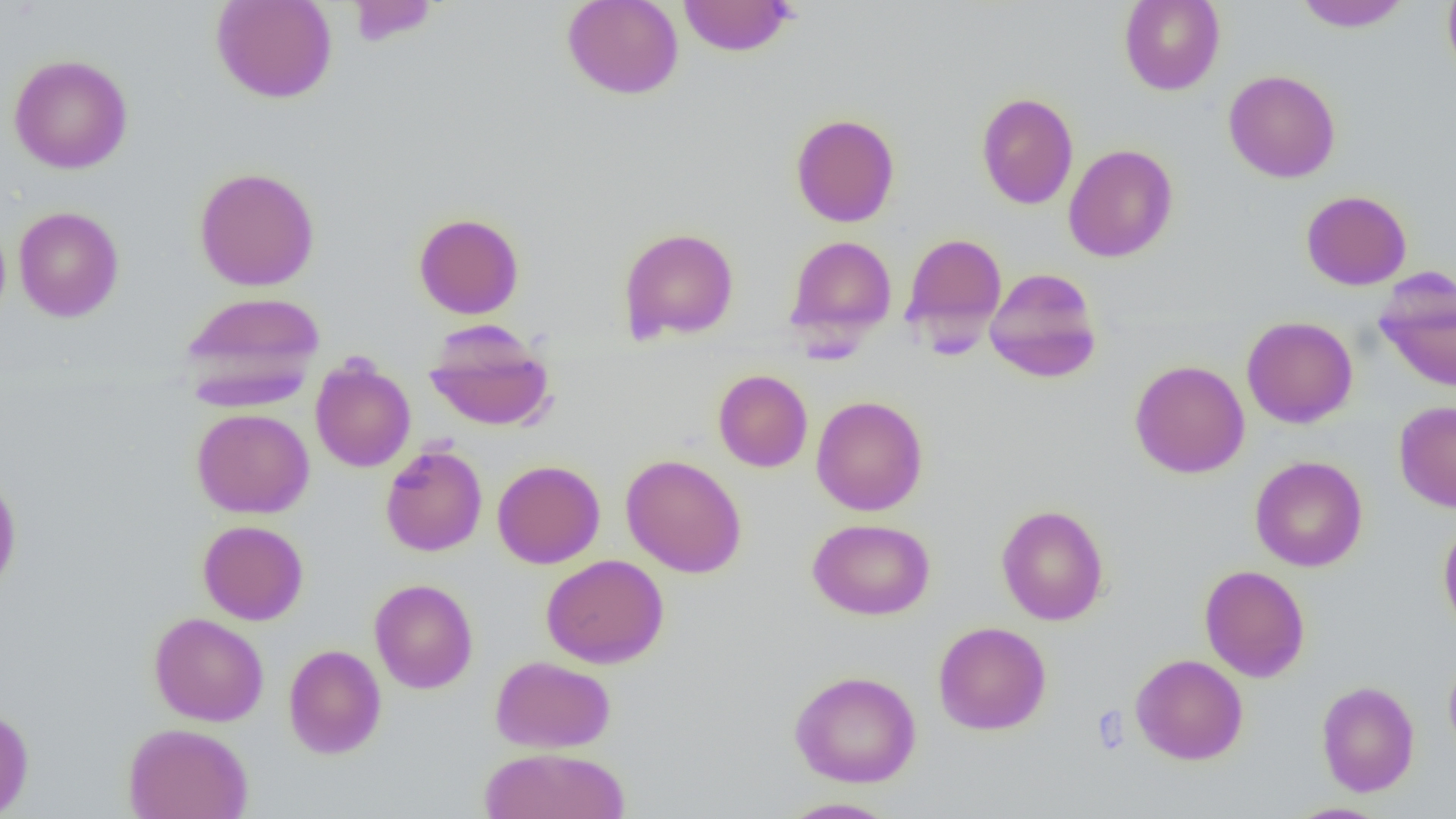

slide-level diagnosis = no evidence of blood parasites
platelet locations = approximate bounding boxes as named x1/y1/x2/y2 corners in pixels: (x1=1090, y1=705, x2=1130, y2=754)
preparation = thin blood film
modality = light microscopy
field of view = single
uninfected red blood cell locations = approximate bounding boxes as named x1/y1/x2/y2 corners in pixels: (x1=210, y1=0, x2=337, y2=104), (x1=561, y1=0, x2=684, y2=100), (x1=677, y1=0, x2=796, y2=57), (x1=1118, y1=0, x2=1225, y2=95), (x1=1294, y1=0, x2=1410, y2=31), (x1=1442, y1=0, x2=1456, y2=84), (x1=346, y1=1, x2=440, y2=46), (x1=8, y1=54, x2=133, y2=174), (x1=1223, y1=69, x2=1341, y2=183), (x1=976, y1=91, x2=1079, y2=210), (x1=790, y1=114, x2=900, y2=227), (x1=1063, y1=143, x2=1178, y2=262), (x1=194, y1=166, x2=320, y2=291), (x1=1301, y1=190, x2=1412, y2=290), (x1=13, y1=206, x2=124, y2=322), (x1=413, y1=212, x2=524, y2=319), (x1=618, y1=227, x2=739, y2=342), (x1=901, y1=232, x2=1007, y2=341), (x1=785, y1=235, x2=897, y2=343), (x1=984, y1=267, x2=1103, y2=383), (x1=1375, y1=273, x2=1456, y2=392), (x1=180, y1=290, x2=325, y2=401), (x1=1242, y1=316, x2=1358, y2=428), (x1=423, y1=322, x2=555, y2=432), (x1=310, y1=357, x2=415, y2=472), (x1=1130, y1=359, x2=1250, y2=479), (x1=713, y1=369, x2=812, y2=473), (x1=811, y1=395, x2=928, y2=516), (x1=1394, y1=401, x2=1456, y2=512), (x1=192, y1=408, x2=314, y2=518), (x1=381, y1=444, x2=487, y2=556), (x1=621, y1=453, x2=747, y2=578), (x1=1250, y1=455, x2=1367, y2=572), (x1=492, y1=460, x2=605, y2=568), (x1=0, y1=472, x2=21, y2=596), (x1=996, y1=504, x2=1109, y2=625), (x1=1438, y1=516, x2=1456, y2=640), (x1=807, y1=518, x2=935, y2=620), (x1=197, y1=520, x2=308, y2=625), (x1=541, y1=554, x2=669, y2=668), (x1=1199, y1=564, x2=1310, y2=682), (x1=369, y1=578, x2=478, y2=694), (x1=148, y1=612, x2=269, y2=726), (x1=932, y1=621, x2=1052, y2=735), (x1=283, y1=644, x2=386, y2=759), (x1=1130, y1=653, x2=1248, y2=765), (x1=1443, y1=653, x2=1456, y2=762), (x1=490, y1=655, x2=616, y2=753), (x1=789, y1=669, x2=922, y2=788), (x1=1316, y1=680, x2=1420, y2=797), (x1=0, y1=707, x2=34, y2=818), (x1=123, y1=722, x2=253, y2=819), (x1=478, y1=746, x2=631, y2=819), (x1=778, y1=797, x2=902, y2=818), (x1=1284, y1=802, x2=1392, y2=819)
magnification = 1000x
image size = 1456×819 pixels